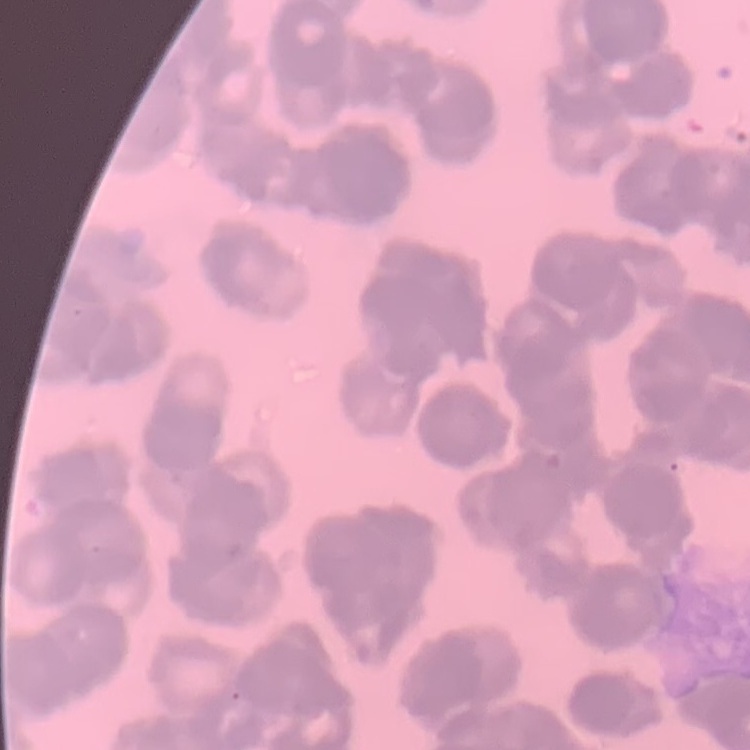
{
  "red_blood_cell_morphology": "rouleaux formation",
  "stain": "Field's or Giemsa",
  "preparation": "thin peripheral smear",
  "image_type": "square crop of a larger photomicrograph"
}